Report the malaria status of this cell.
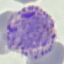

Parasitized.

capture: smartphone camera at the microscope eyepiece
preparation: thin blood film
image_type: automatically extracted cell patch, resized to 64 × 64 pixels
stain: Giemsa